Name the parasite shown.
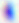
This is Toxoplasma gondii.

Photomicrograph. Captured at 400x magnification.